Look for Plasmodium parasites.
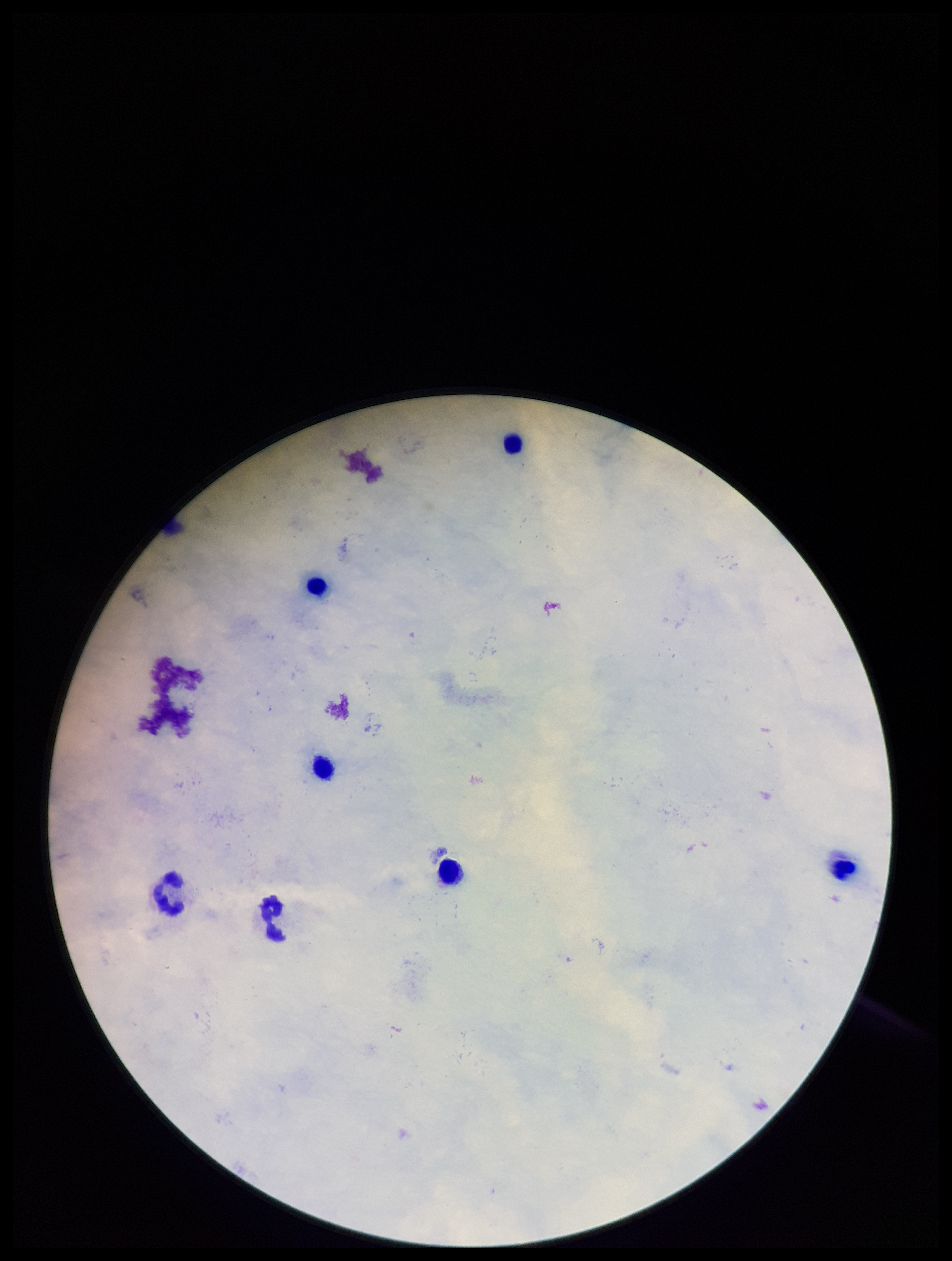

None seen.

patient malaria status = negative
image size = 952×1261 pixels
preparation = thick smear
field of view = single
capture = smartphone photograph through the microscope eyepiece
parasite count = 0
leukocyte count = 7
stain = Giemsa